Report the malaria status of this cell.
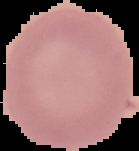
It is uninfected.

From a thin blood film. Image is 139×151 pixels. Segmented cell region on a black background.